State which parasite is depicted.
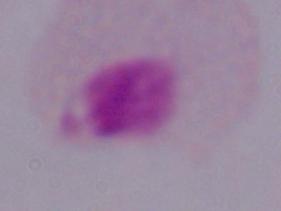
This is a trichomonad.

Photomicrograph. Captured at 1000x magnification.